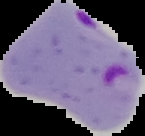
From a thin blood film. Image is 145×136 pixels. Result: Plasmodium parasites detected. Segmented cell region on a black background.